Name the cell type shown.
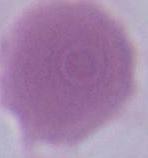

An erythrocyte.

modality = photomicrograph
magnification = 1000x